Report the malaria status of this cell.
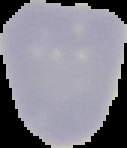
Uninfected.

image type = segmented cell region on a black background
preparation = thin blood smear
image size = 127×148 pixels